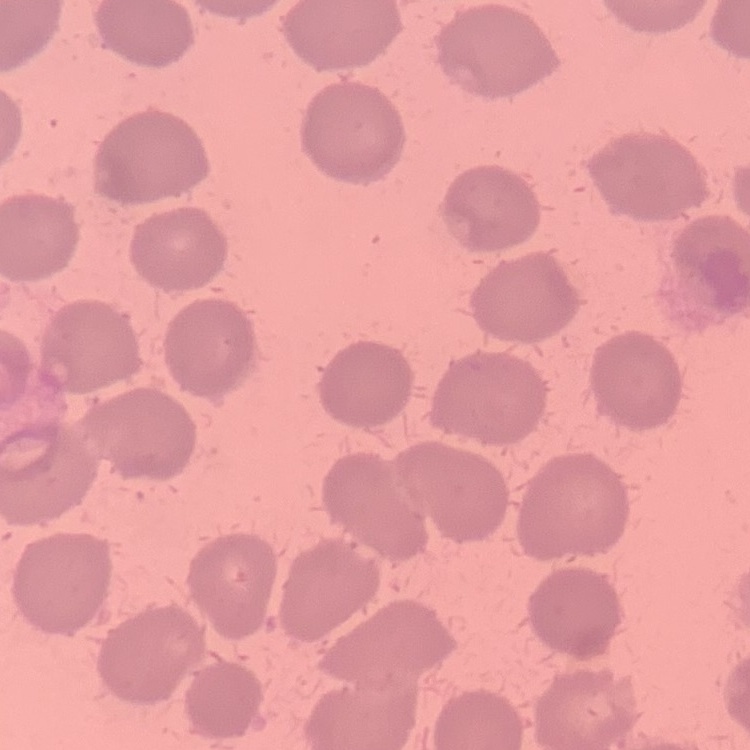
red blood cell morphology = no rouleaux formation
preparation = thin blood smear
stain = Field's or Giemsa
image type = one tile cut from a larger photomicrograph